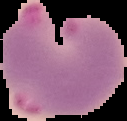

Summary:
  - Image size: 127×121 pixels
  - Image type: segmented cell region with the area outside set to black
  - Result: malaria parasites detected
  - Preparation: thin blood smear